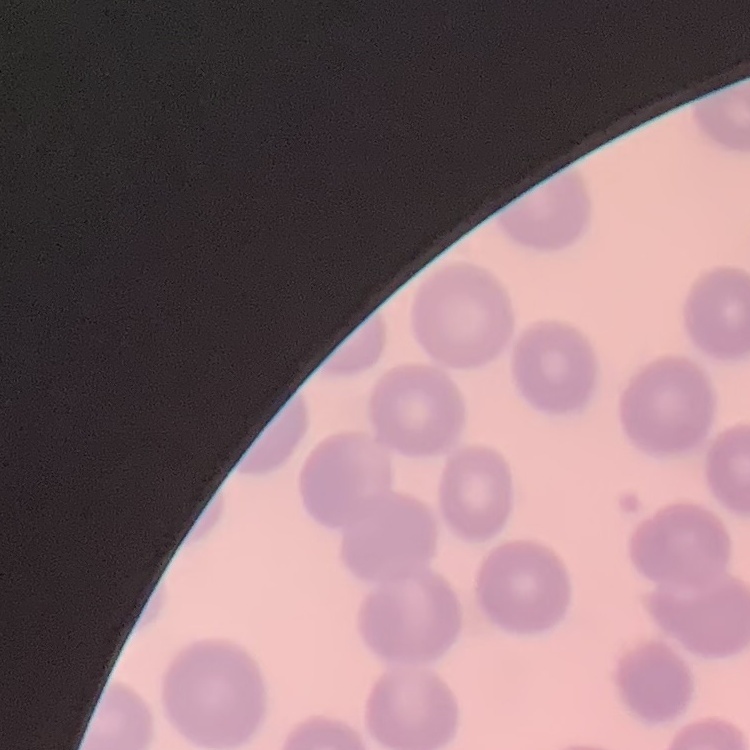

The erythrocytes show no rouleaux formation. One tile cut from a larger photomicrograph. Thin blood smear. Field's or Giemsa stain.